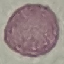
Summary:
  - Malaria status: uninfected
  - Preparation: thin blood film
  - Capture: smartphone through the microscope eyepiece
  - Stain: Giemsa
  - Image type: cell patch, automatically extracted from a larger field of view and resized to 64 × 64 pixels